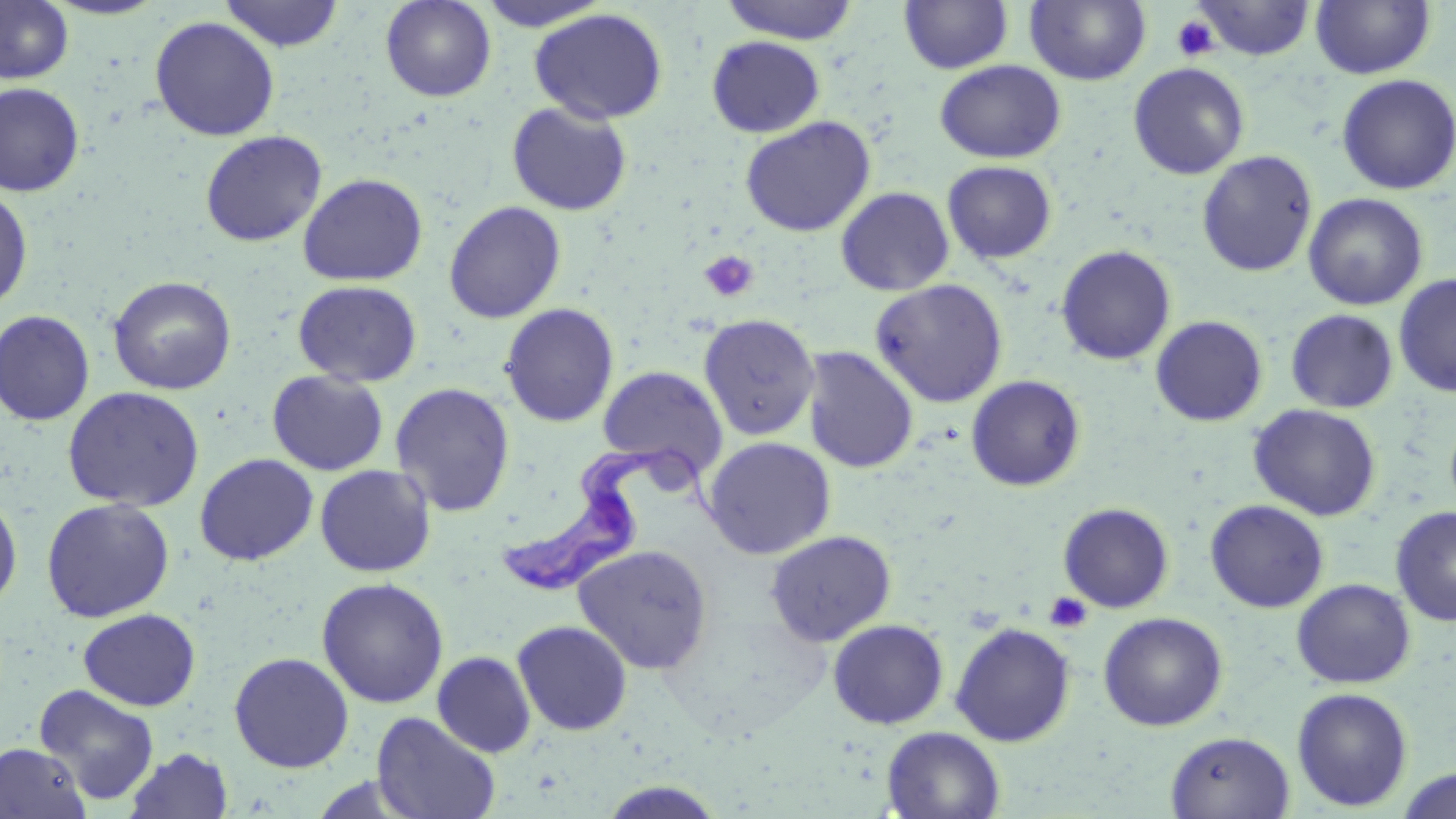

Approximate bounding boxes as (x1,y1)-(x2,y2) corner pairs in pixels. Uninfected red blood cell locations: (0,0)-(74,85), (41,0)-(170,20), (219,0)-(345,52), (380,0)-(496,102), (475,0)-(613,31), (719,0)-(860,44), (899,0)-(1014,75), (1024,0)-(1151,86), (1192,0)-(1315,61), (1311,0)-(1435,79), (530,8)-(668,124), (149,16)-(280,141), (706,35)-(825,138), (934,60)-(1066,164), (1128,62)-(1249,179), (1336,74)-(1455,195), (0,83)-(84,197), (506,101)-(632,216), (740,115)-(876,237), (200,130)-(327,247), (1197,150)-(1318,276), (942,161)-(1057,263), (298,173)-(428,286), (0,187)-(33,312), (835,187)-(954,296), (1303,193)-(1428,311), (444,201)-(566,323), (1055,245)-(1176,366), (1394,273)-(1456,397), (108,275)-(236,395), (871,279)-(1008,407), (293,280)-(422,387), (499,303)-(620,427), (1286,309)-(1399,413), (0,310)-(95,426), (698,313)-(820,440), (1150,315)-(1268,427), (801,346)-(919,474), (597,365)-(727,477), (267,369)-(388,476), (966,375)-(1086,491), (389,382)-(515,518), (62,385)-(204,512), (1248,404)-(1381,521), (702,436)-(836,559), (194,453)-(319,566), (314,464)-(436,577), (0,491)-(23,614), (41,497)-(175,622), (1205,499)-(1329,613), (1058,502)-(1174,613), (1390,506)-(1456,627), (765,530)-(897,647), (572,543)-(713,675), (316,577)-(449,709), (1291,578)-(1415,689), (79,608)-(201,711), (1098,611)-(1227,731), (828,619)-(949,729), (512,620)-(633,736), (950,622)-(1076,747), (229,651)-(354,773), (432,651)-(536,757), (33,684)-(160,804), (1291,687)-(1413,812), (371,711)-(501,819), (882,726)-(1005,818), (1165,731)-(1295,818), (0,742)-(91,818), (126,747)-(234,819), (1394,768)-(1456,819), (597,780)-(729,817). Platelet locations: (1172,14)-(1220,61), (699,251)-(759,303), (1044,592)-(1093,634). Trypanosoma brucei locations: (499,448)-(721,597). Slide-level diagnosis: Trypanosoma brucei. Thin blood smear. May-Grünwald-Giemsa-stained preparation. Single field of view. Optical microscopy. Image is 1456×819 pixels. Captured at 1000x magnification.